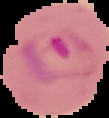
Summary:
  - Malaria status: parasitized
  - Image size: 109×118 pixels
  - Preparation: thin blood smear
  - Image type: segmented cell region on a black background